Name the parasite shown.
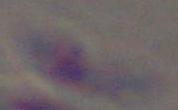
Toxoplasma gondii.

1000x magnification. Micrograph.